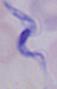

Summary:
  - Identification: trypanosome
  - Magnification: 1000x
  - Modality: micrograph